Describe the morphology of the red blood cells.
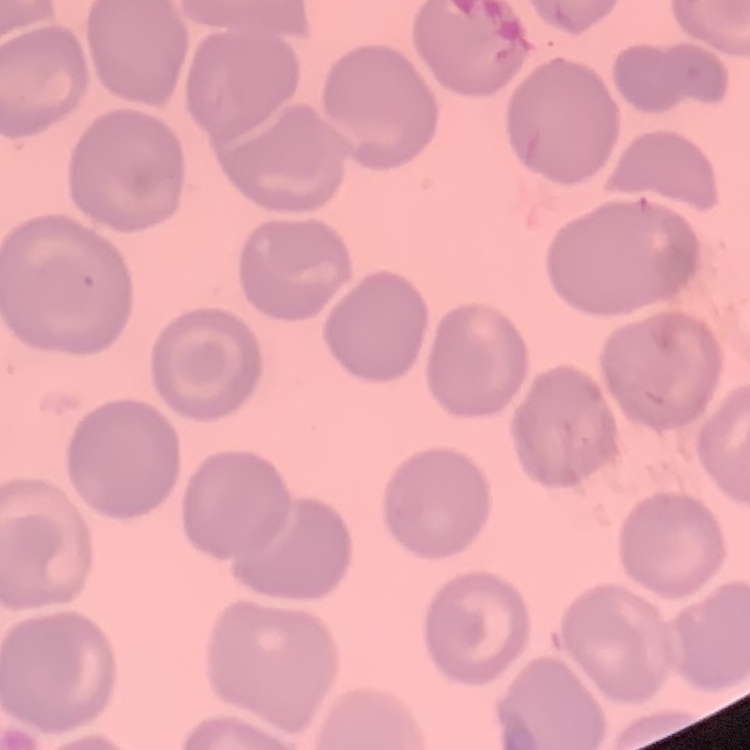
They show no rouleaux formation.

Thin peripheral smear. Square crop of a larger photomicrograph. Field's or Giemsa stain.